Name the parasite shown.
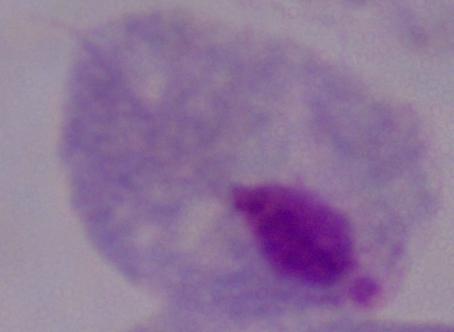
This is a trichomonad.

Summary:
  - Modality: micrograph
  - Magnification: 1000x